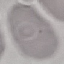
Summary:
  - Result: negative for malaria parasites
  - Capture: smartphone through the microscope eyepiece
  - Stain: Giemsa
  - Image type: cell patch, automatically extracted from a larger field of view and resized to 64 × 64 pixels
  - Preparation: thin smear